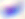

Summary:
  - Magnification: 400x
  - Modality: photomicrograph
  - Identification: Toxoplasma gondii